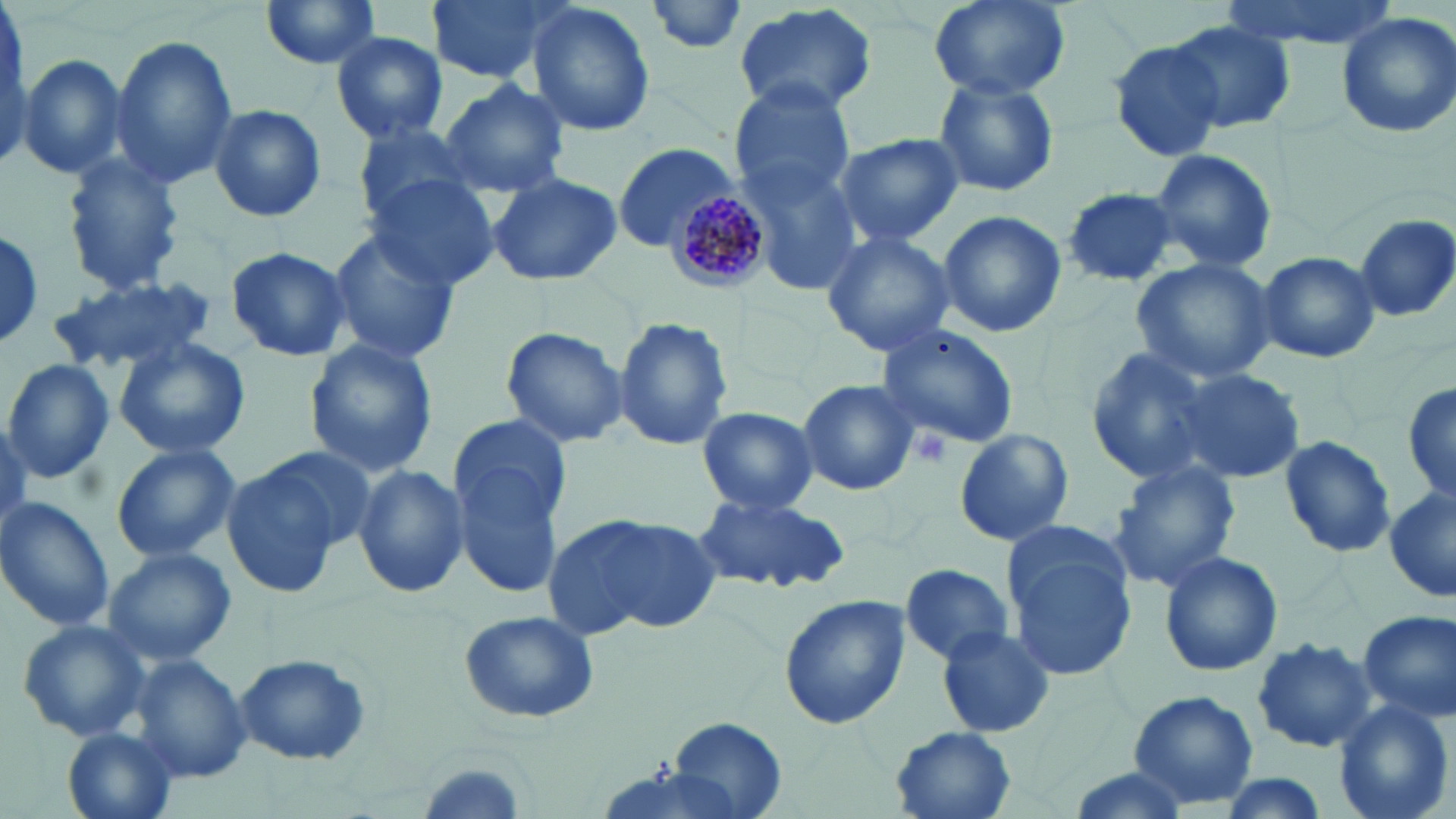

Summary:
  - Coordinate format: approximate bounding boxes as (x1,y1)-(x2,y2) corner pairs in pixels
  - Uninfected red blood cell locations: (426,0)-(568,85), (928,0)-(1068,99), (1214,0)-(1398,50), (258,1)-(384,71), (646,1)-(751,54), (526,3)-(656,139), (732,4)-(879,120), (1335,11)-(1456,139), (0,13)-(33,171), (1164,20)-(1295,133), (331,32)-(448,143), (110,37)-(239,186), (1107,37)-(1226,162), (17,53)-(127,181), (931,77)-(1060,198), (438,78)-(570,198), (729,82)-(856,204), (206,103)-(326,222), (350,120)-(484,228), (832,133)-(964,246), (614,143)-(739,251), (1149,148)-(1277,275), (740,153)-(869,291), (61,155)-(184,294), (487,172)-(623,286), (366,175)-(502,291), (1059,187)-(1182,287), (937,210)-(1067,339), (1353,214)-(1456,321), (1,225)-(45,349), (324,227)-(463,364), (820,231)-(956,357), (222,247)-(352,360), (1255,250)-(1380,363), (1131,256)-(1278,385), (53,276)-(212,371), (614,315)-(734,453), (875,323)-(1020,451), (500,325)-(629,449), (113,337)-(251,459), (302,339)-(439,479), (1083,346)-(1219,487), (2,358)-(114,484), (1169,365)-(1305,484), (797,379)-(920,497), (1403,381)-(1456,503), (697,406)-(818,514), (447,417)-(575,596), (953,425)-(1074,548), (1277,435)-(1393,556), (110,444)-(240,563), (223,453)-(362,597), (1110,461)-(1240,591), (351,463)-(470,599), (1385,487)-(1455,604), (693,491)-(850,593), (0,497)-(114,633), (553,512)-(717,636), (1000,520)-(1137,680), (104,546)-(236,667), (1158,551)-(1283,678), (899,561)-(1013,666), (778,597)-(910,729), (458,610)-(599,723), (1356,610)-(1456,722), (16,618)-(152,744), (935,626)-(1055,738), (1250,637)-(1378,753), (233,653)-(372,766), (131,655)-(252,782), (1126,690)-(1258,809), (1334,700)-(1453,819), (666,716)-(788,817), (889,727)-(1016,819), (63,728)-(179,819), (1205,773)-(1337,819)
  - Plasmodium malariae-infected red blood cell locations: (664,184)-(775,291)
  - Platelet locations: (909,428)-(952,470)
  - Slide-level diagnosis: Plasmodium malariae
  - Image size: 1456×819 pixels
  - Field of view: one of a larger specimen
  - Stain: May-Grünwald-Giemsa
  - Modality: optical microscopy
  - Magnification: 1000x
  - Preparation: thin blood film